Classify this cell by malaria status.
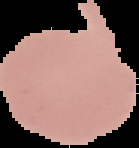

It is uninfected.

Summary:
  - Preparation: thin blood smear
  - Image type: segmented cell region on a black background
  - Image size: 139×148 pixels